Give a bounding box for every leukocyte visible.
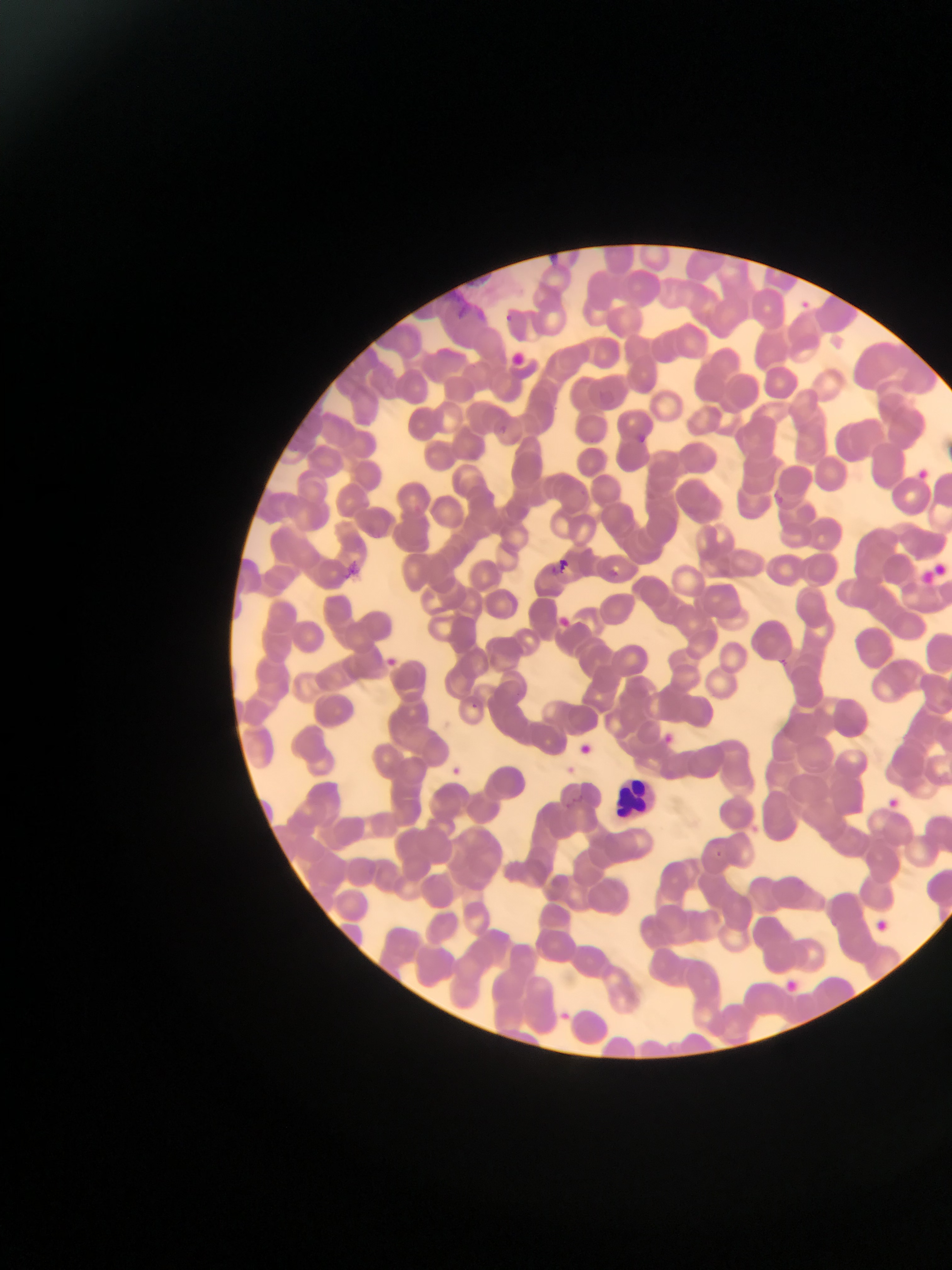
Approximate bounding boxes as [left, top, right, bottom] in pixels.
Leukocytes: [607, 767, 670, 817].

Summary:
  - Plasmodium parasite locations: [797, 298, 808, 308], [505, 311, 517, 323], [635, 428, 655, 448], [775, 488, 785, 505], [556, 555, 575, 572], [609, 567, 624, 578], [560, 616, 577, 630], [385, 652, 401, 667], [780, 657, 794, 670], [471, 700, 488, 714], [666, 730, 674, 739], [560, 762, 574, 779], [453, 766, 468, 775], [885, 795, 908, 814], [713, 844, 724, 858], [874, 919, 890, 933], [782, 977, 802, 991], [562, 1011, 577, 1022]
  - Preparation: thin blood smear
  - Field of view: single
  - Capture: mobile-phone photograph through a microscope
  - Country: Ghana
  - Image size: 952×1270 pixels